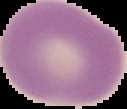

Summary:
  - Preparation: thin blood film
  - Image type: segmented cell region with the area outside set to black
  - Result: no malaria parasites detected
  - Image size: 127×109 pixels